Locate every Trypanosoma brucei.
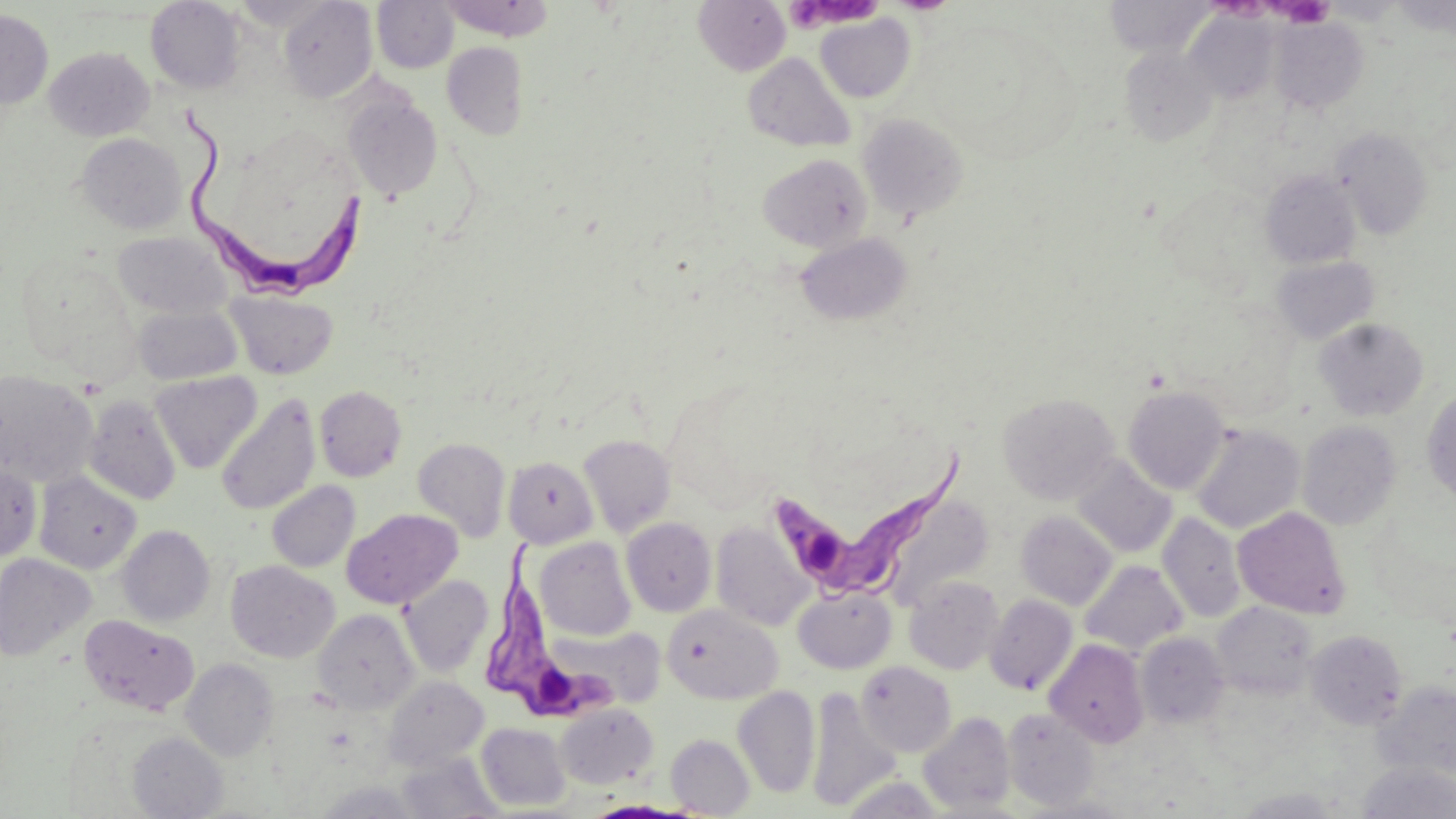
Approximate bounding boxes as (x1,y1)-(x2,y2) corner pairs in pixels.
Trypanosoma brucei: (181,106)-(369,296), (776,448)-(965,601), (484,539)-(619,725).

Uninfected red blood cell locations: (438,0)-(555,41), (693,0)-(791,76), (1103,0)-(1216,56), (146,1)-(246,94), (278,1)-(377,103), (371,1)-(458,73), (0,9)-(53,109), (1183,10)-(1279,105), (815,14)-(915,103), (1271,18)-(1369,113), (441,42)-(529,140), (1120,43)-(1221,147), (44,47)-(153,141), (744,52)-(855,153), (341,87)-(443,202), (857,114)-(969,221), (1331,127)-(1434,239), (77,133)-(186,234), (758,154)-(872,253), (1260,170)-(1361,269), (112,231)-(233,319), (795,232)-(913,326), (1271,255)-(1379,344), (227,290)-(337,379), (133,304)-(242,385), (1314,317)-(1429,421), (0,370)-(99,487), (150,371)-(262,474), (314,385)-(407,482), (1123,385)-(1230,495), (1421,388)-(1456,504), (999,392)-(1120,505), (83,394)-(181,505), (216,395)-(320,516), (1297,420)-(1402,530), (1191,424)-(1304,534), (578,434)-(676,538), (412,437)-(511,542), (503,456)-(598,549), (1072,457)-(1176,558), (0,462)-(41,561), (35,472)-(141,575), (267,481)-(360,572), (881,491)-(993,610), (1233,507)-(1351,619), (342,508)-(462,609), (1016,510)-(1117,610), (1157,512)-(1245,622), (621,517)-(717,616), (710,521)-(812,631), (117,525)-(215,626), (534,537)-(636,641), (0,553)-(96,661), (226,560)-(339,662), (1079,560)-(1188,656), (399,575)-(493,676), (904,575)-(1004,675), (793,587)-(896,674), (984,594)-(1078,694), (1212,602)-(1317,698), (663,604)-(783,704), (312,608)-(419,714), (79,614)-(200,717), (554,625)-(666,709), (1305,630)-(1408,730), (1136,633)-(1230,728), (1044,639)-(1149,747), (181,658)-(278,761), (856,661)-(956,756), (382,676)-(488,770), (1373,682)-(1456,783), (733,685)-(820,798), (805,687)-(902,811), (555,703)-(658,789), (1001,708)-(1101,811), (917,711)-(1016,814), (476,722)-(571,811), (127,732)-(227,818), (666,733)-(754,816), (396,753)-(503,819), (1356,761)-(1456,819), (1234,788)-(1344,818). Platelet locations: (788,0)-(882,35), (1227,0)-(1327,25). Slide-level diagnosis: Trypanosoma brucei. Captured at 1000x magnification. Light microscopy. Single field of view. Thin blood film. Image is 1456×819 pixels. May-Grünwald-Giemsa-stained preparation.